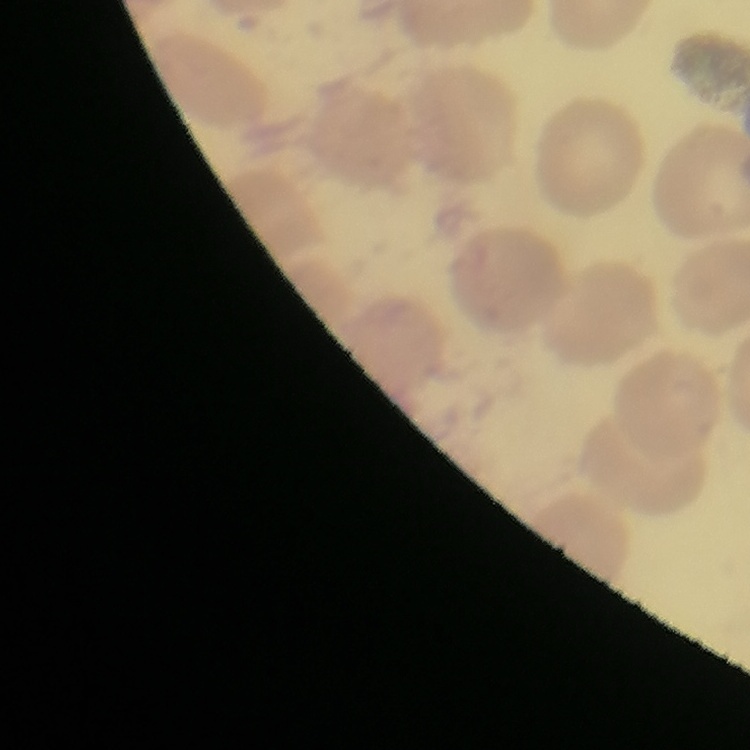

red blood cell morphology = no rouleaux formation
preparation = thin blood smear
stain = Field's or Giemsa
image type = square crop of a larger photomicrograph